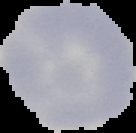
{
  "malaria_status": "uninfected",
  "image_size": "136×133 pixels",
  "image_type": "segmented cell region with the area outside set to black",
  "preparation": "thin blood smear"
}